Give the preparation type.
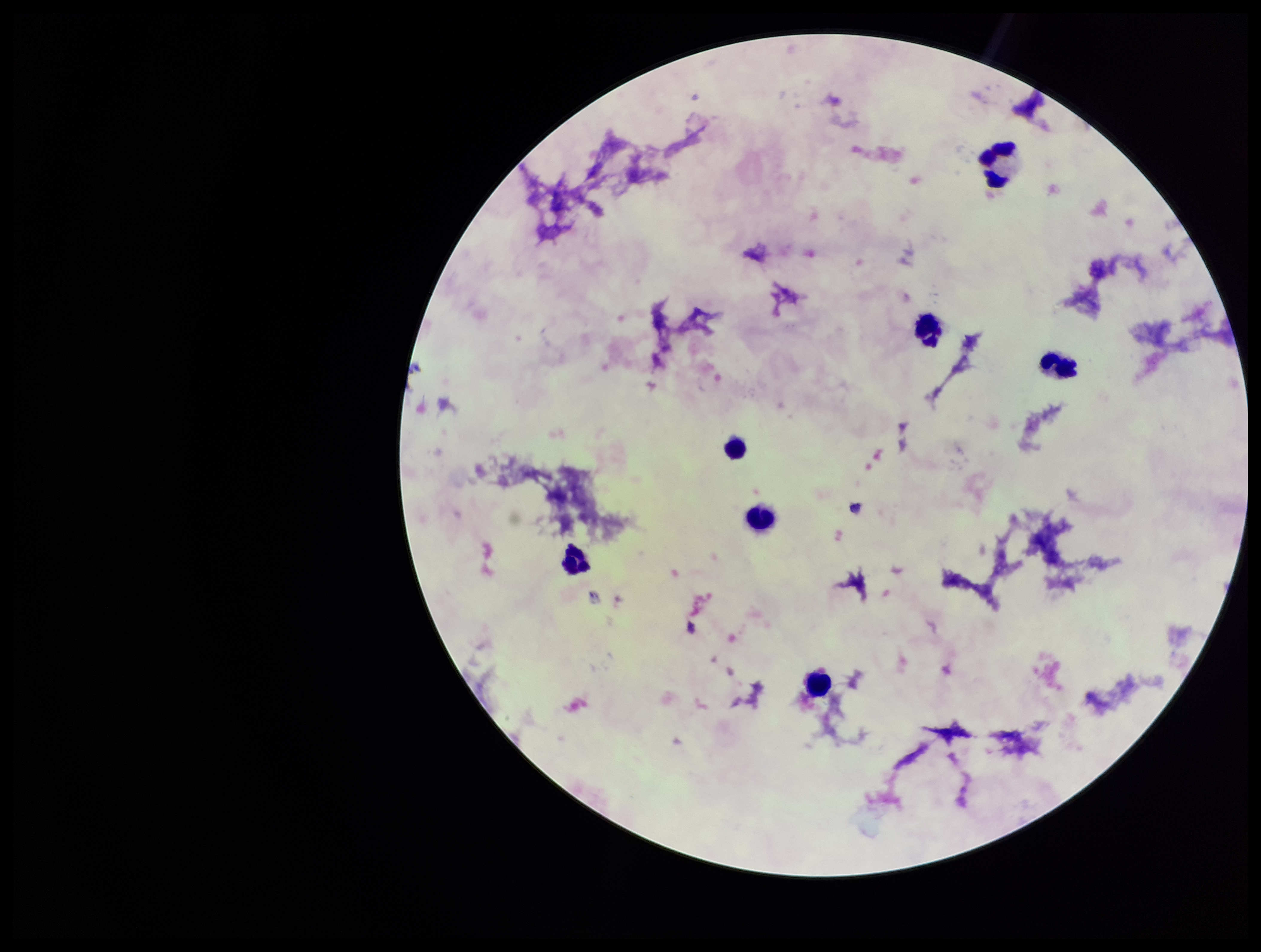

A thick smear.

patient malaria status = negative
field of view = single
capture = smartphone photograph through the microscope eyepiece
stain = Giemsa
image size = 1261×952 pixels
Plasmodium parasites = none identified
parasite count = 0
leukocyte count = 7